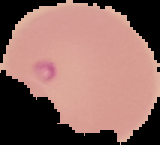
Summary:
  - Preparation: thin blood film
  - Image type: segmented cell region with the area outside set to black
  - Malaria status: parasitized
  - Image size: 160×145 pixels